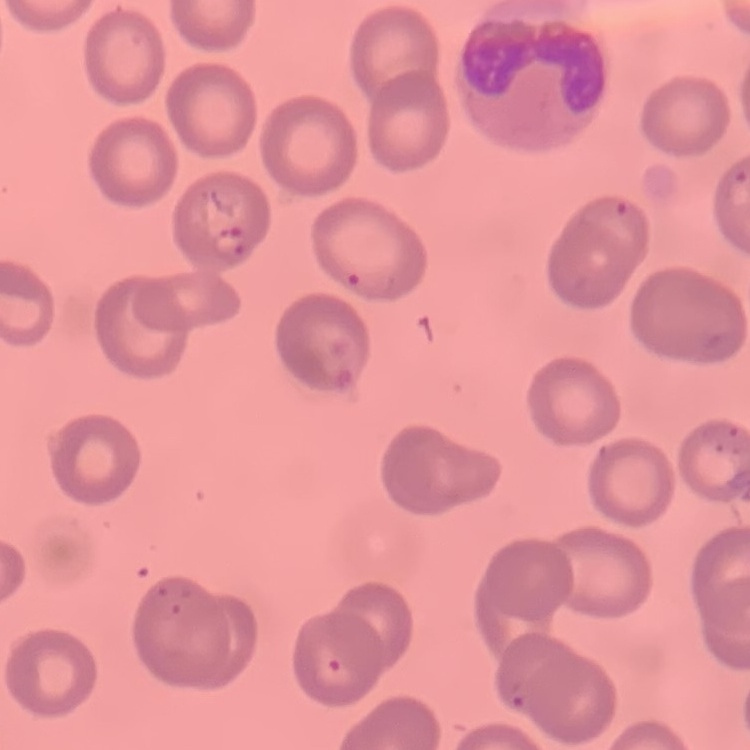
red_blood_cell_morphology: no rouleaux formation
image_type: square crop of a larger photomicrograph
stain: Field's or Giemsa
preparation: thin blood smear